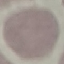

Summary:
  - Malaria status: uninfected
  - Preparation: thin blood smear
  - Capture: smartphone through the microscope eyepiece
  - Image type: automatically extracted cell patch, resized to 64 × 64 pixels
  - Stain: Giemsa